Outline platelets.
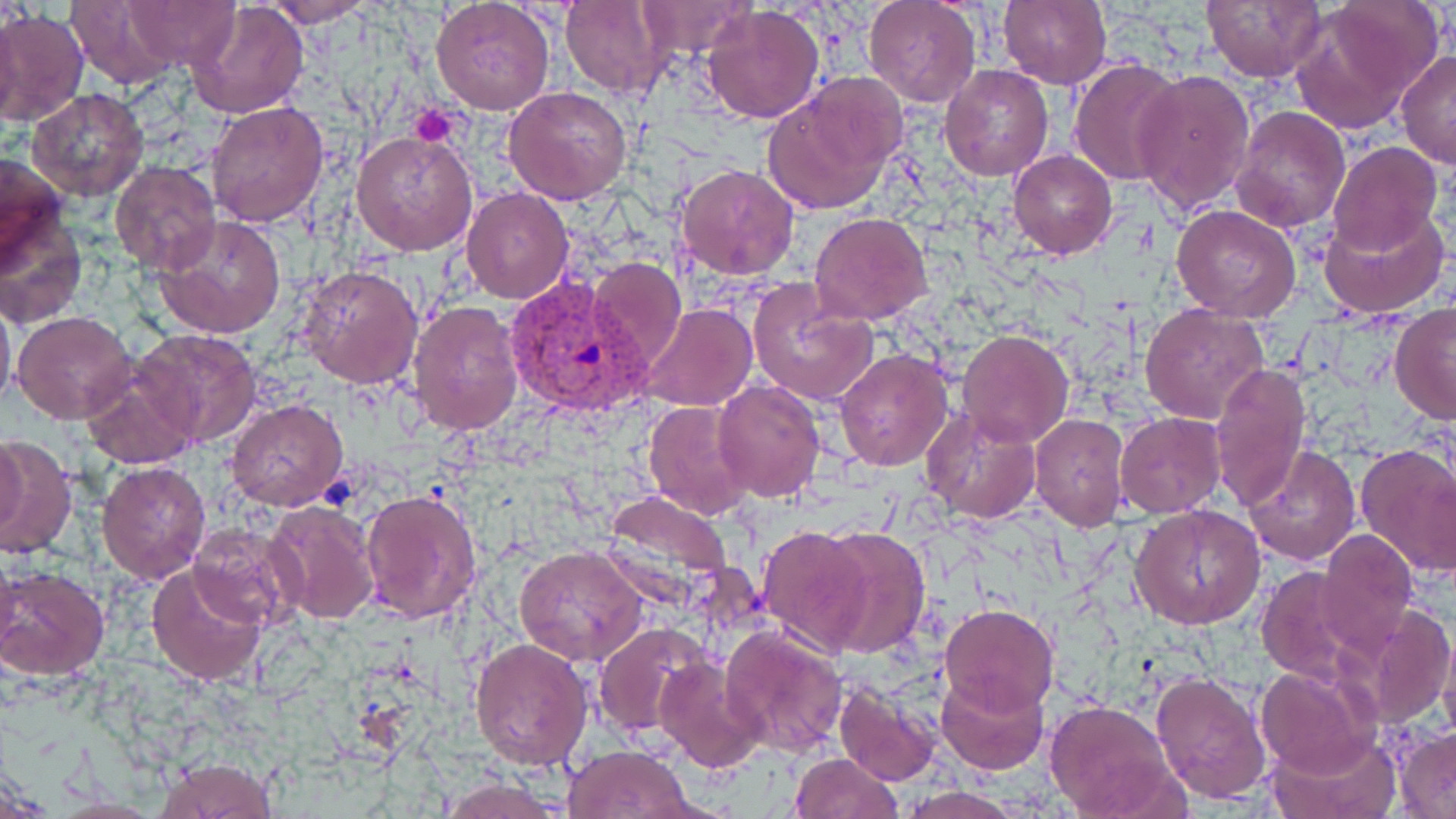

Approximate bounding boxes as [x1, y1, x2, y2] in pixels.
Platelets: [410, 104, 464, 145].

Plasmodium vivax-infected red blood cell locations: [504, 276, 653, 417]. Uninfected red blood cell locations: [122, 0, 239, 68], [261, 0, 380, 25], [561, 0, 671, 99], [638, 0, 757, 58], [863, 0, 981, 108], [996, 0, 1112, 90], [1202, 0, 1325, 83], [64, 1, 180, 88], [185, 1, 310, 118], [431, 1, 557, 115], [1289, 1, 1442, 134], [701, 4, 824, 124], [0, 8, 87, 126], [1396, 50, 1456, 170], [1067, 58, 1187, 186], [939, 65, 1054, 182], [1131, 67, 1256, 215], [759, 83, 902, 216], [504, 84, 633, 205], [25, 88, 147, 202], [206, 101, 329, 228], [1230, 106, 1350, 233], [351, 129, 478, 256], [1329, 141, 1442, 257], [1008, 148, 1117, 259], [2, 152, 72, 274], [109, 162, 222, 275], [675, 162, 800, 280], [460, 186, 572, 304], [1170, 203, 1302, 322], [0, 207, 86, 330], [1320, 207, 1449, 319], [809, 212, 932, 324], [155, 215, 287, 340], [586, 256, 687, 372], [297, 263, 424, 390], [747, 278, 879, 407], [0, 293, 15, 416], [407, 299, 523, 436], [1141, 301, 1270, 425], [641, 303, 757, 412], [1389, 303, 1456, 425], [12, 311, 136, 425], [136, 327, 263, 449], [955, 329, 1073, 447], [834, 349, 953, 471], [82, 362, 198, 473], [1209, 362, 1313, 513], [713, 378, 825, 502], [225, 398, 348, 512], [644, 400, 755, 521], [921, 405, 1042, 525], [1028, 412, 1131, 530], [1115, 412, 1224, 517], [1, 431, 30, 546], [0, 434, 76, 560], [1354, 442, 1456, 581], [1244, 445, 1360, 566], [97, 462, 212, 583], [360, 488, 483, 623], [601, 491, 734, 601], [264, 501, 381, 623], [1131, 505, 1265, 629], [187, 522, 305, 632], [757, 527, 872, 653], [814, 528, 930, 660], [1313, 532, 1419, 664], [514, 545, 650, 668], [146, 562, 269, 687], [1255, 565, 1370, 687], [0, 566, 110, 680], [1366, 602, 1455, 730], [940, 604, 1058, 715], [594, 621, 712, 736], [719, 623, 848, 755], [468, 637, 594, 771], [656, 657, 769, 771], [1255, 665, 1380, 780], [936, 670, 1048, 774], [1151, 670, 1272, 805], [833, 685, 941, 786], [1044, 700, 1187, 818], [1393, 729, 1456, 816], [1266, 730, 1398, 818], [563, 744, 696, 818], [789, 751, 904, 819], [155, 758, 277, 818], [437, 778, 569, 818], [893, 787, 1034, 819]. Slide-level diagnosis: Plasmodium vivax. 1000x magnification. Single field of view. Thin blood film. Optical microscopy. Image is 1456×819 pixels. May-Grünwald-Giemsa stain.